Outline each Plasmodium ovale-infected red blood cell.
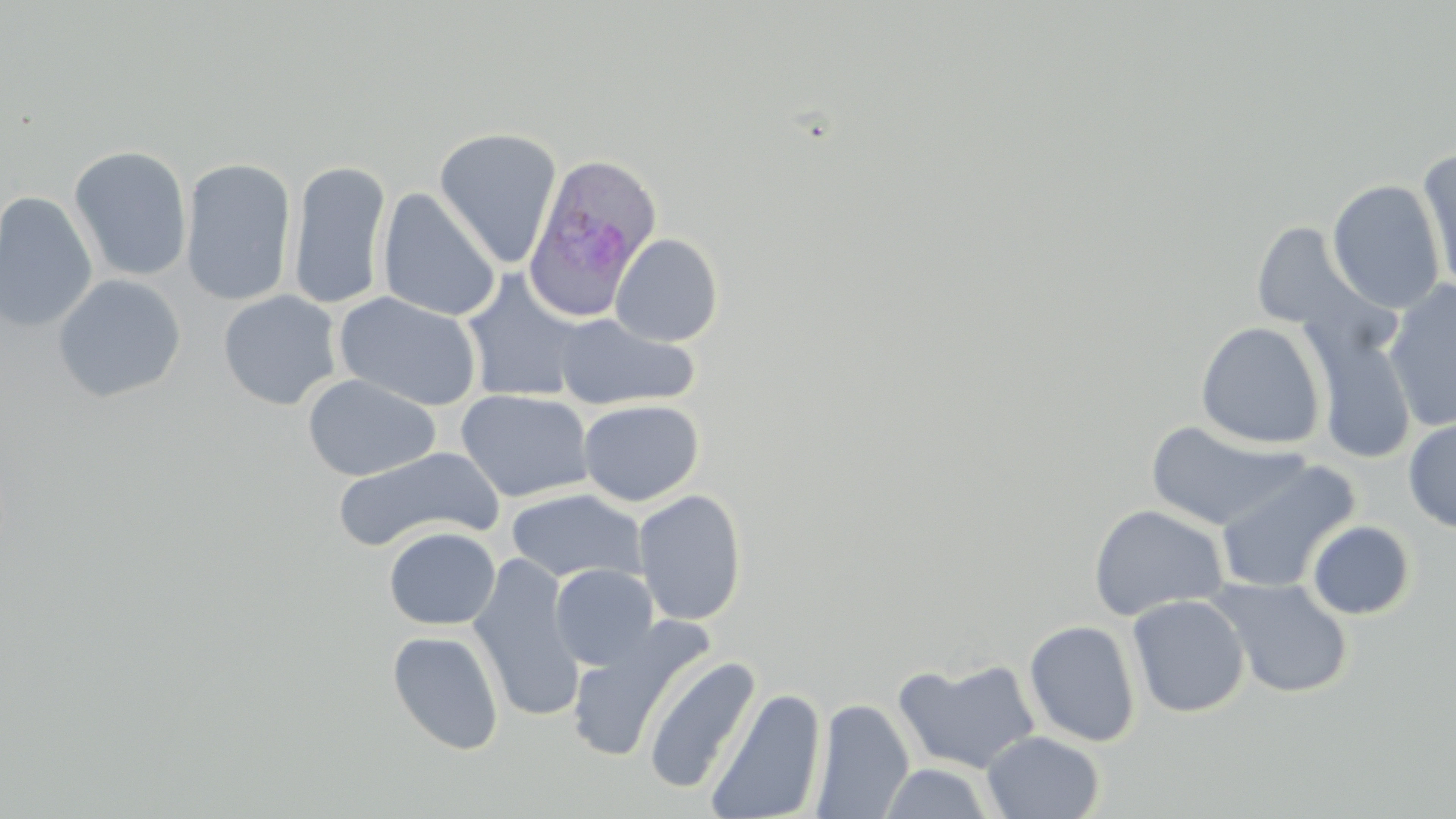
Approximate bounding boxes as (x1,y1)-(x2,y2) corner pairs in pixels.
Plasmodium ovale-infected red blood cells: (521,152)-(663,322).

slide-level diagnosis = Plasmodium ovale
field of view = one of a larger specimen
stain = May-Grünwald-Giemsa
image size = 1456×819 pixels
magnification = 1000x
modality = light microscopy
uninfected red blood cell locations = approximate bounding boxes as (x1,y1)-(x2,y2) corner pairs in pixels: (434,127)-(562,268), (68,144)-(193,283), (1415,150)-(1455,292), (180,156)-(297,307), (287,159)-(392,310), (1327,179)-(1445,314), (377,188)-(501,322), (0,191)-(98,333), (1249,221)-(1373,338), (610,233)-(724,347), (460,270)-(589,403), (52,274)-(186,403), (1384,281)-(1456,433), (218,289)-(343,410), (334,291)-(483,412), (553,313)-(699,411), (1303,319)-(1418,465), (1195,321)-(1326,450), (303,374)-(440,481), (457,388)-(594,503), (578,399)-(704,506), (1403,415)-(1456,533), (1144,420)-(1307,531), (332,446)-(502,553), (1214,458)-(1360,595), (505,488)-(646,585), (632,488)-(748,626), (1088,504)-(1229,621), (1306,520)-(1416,620), (383,527)-(501,631), (468,554)-(585,722), (550,564)-(659,671), (1206,576)-(1354,699), (1126,593)-(1250,718), (565,618)-(714,764), (1024,619)-(1141,747), (387,630)-(505,756), (642,654)-(762,795), (893,658)-(1042,775), (705,687)-(826,819), (810,698)-(914,819), (982,731)-(1105,818), (878,763)-(997,819)
preparation = thin blood film